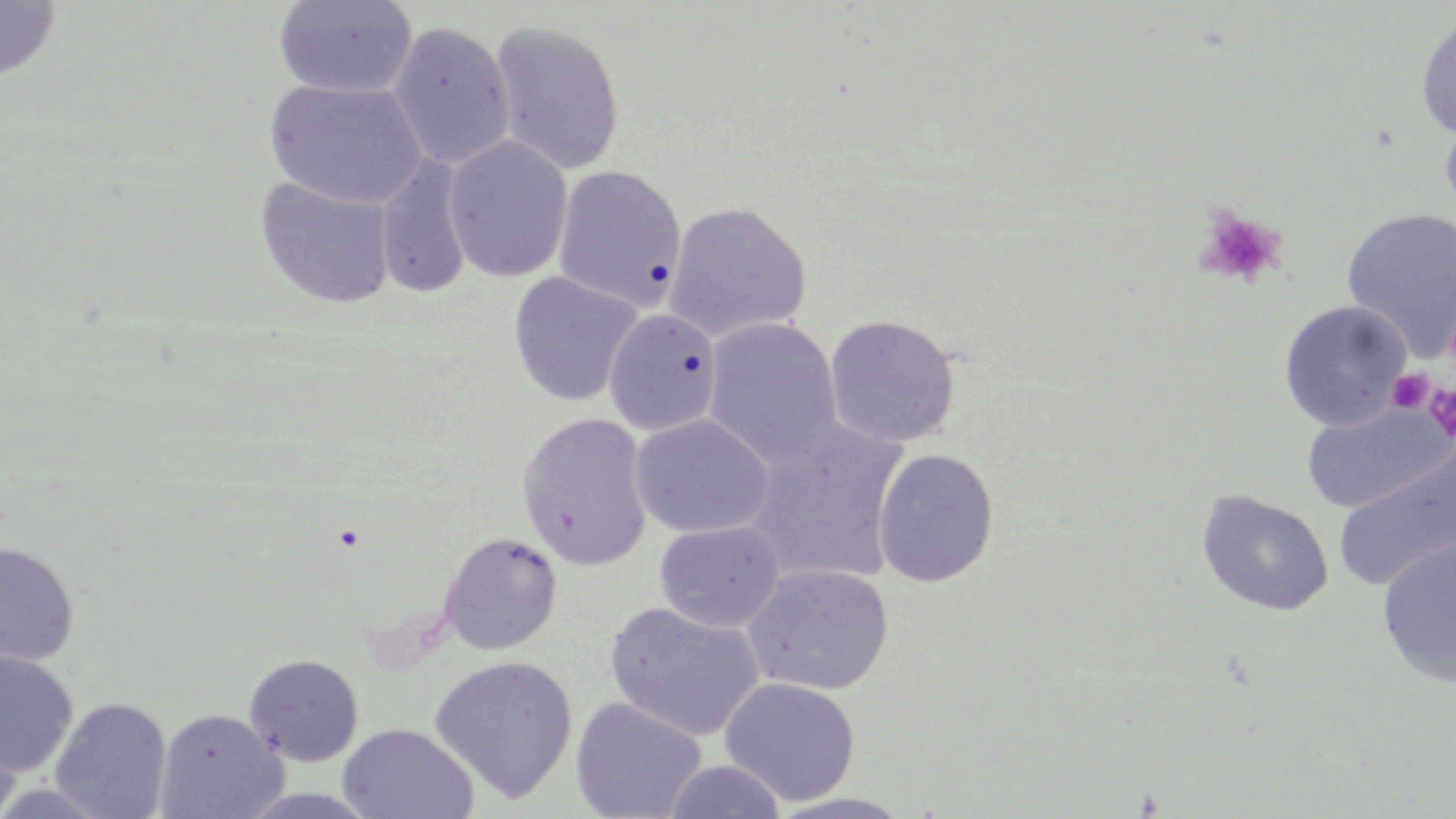
Summary:
  - Coordinate format: approximate bounding boxes as [x1, y1, x2, y2] in pixels
  - Uninfected red blood cell locations: [273, 0, 417, 99], [0, 1, 61, 84], [1415, 13, 1456, 140], [487, 19, 626, 176], [386, 21, 517, 170], [263, 77, 430, 210], [1439, 111, 1456, 227], [442, 134, 574, 284], [375, 154, 472, 299], [552, 164, 688, 311], [254, 176, 397, 310], [663, 201, 812, 344], [1341, 208, 1456, 358], [507, 270, 645, 408], [1278, 300, 1413, 432], [603, 309, 723, 437], [822, 312, 961, 449], [702, 317, 843, 469], [1301, 400, 1454, 514], [515, 412, 653, 571], [629, 414, 774, 539], [744, 421, 909, 586], [1333, 442, 1455, 593], [872, 447, 999, 587], [1197, 490, 1334, 616], [654, 519, 785, 632], [439, 531, 563, 655], [1377, 537, 1456, 689], [0, 541, 80, 666], [740, 563, 894, 696], [603, 601, 766, 742], [0, 649, 78, 777], [243, 653, 365, 767], [428, 655, 579, 803], [718, 676, 861, 806], [50, 696, 173, 818], [570, 696, 707, 819], [154, 707, 287, 819], [0, 714, 23, 819], [338, 723, 479, 818], [661, 759, 787, 819]
  - Platelet locations: [1192, 206, 1286, 288], [1387, 369, 1434, 414], [1424, 384, 1456, 444]
  - Slide-level diagnosis: no evidence of blood parasites
  - Magnification: 1000x
  - Modality: optical microscopy
  - Preparation: thin blood smear
  - Image size: 1456×819 pixels
  - Field of view: one of a larger specimen
  - Stain: May-Grünwald-Giemsa